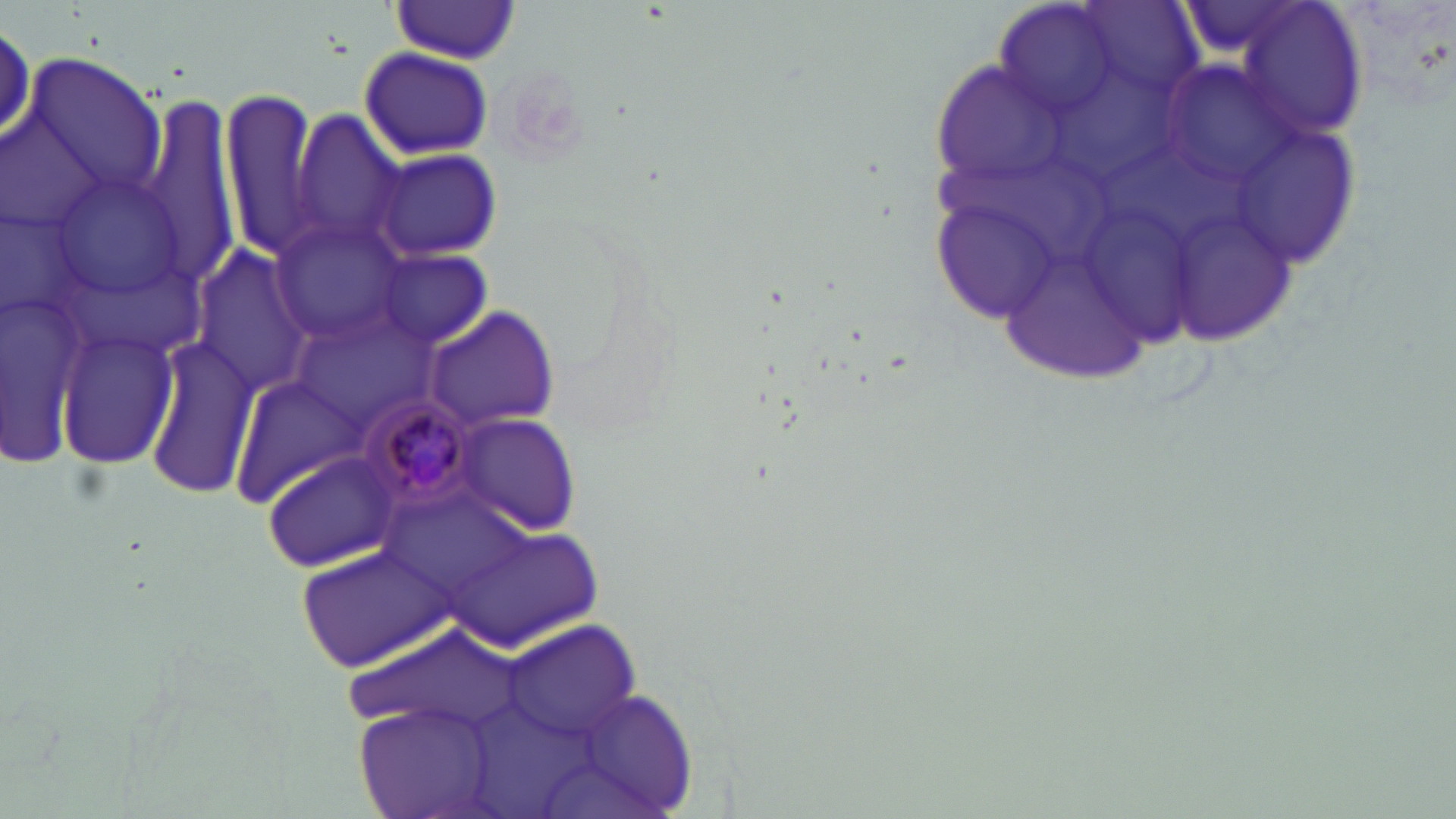 Approximate bounding boxes as (x1,y1)-(x2,y2) corner pairs in pixels. Plasmodium malariae-infected red blood cell locations: (357,390)-(484,510). Uninfected red blood cell locations: (1225,0)-(1367,142), (385,3)-(524,64), (359,47)-(493,160), (23,53)-(164,204), (141,90)-(241,274), (220,90)-(325,262), (290,110)-(410,257), (370,146)-(504,262), (933,197)-(1064,323), (270,217)-(411,340), (190,244)-(315,396), (374,250)-(495,348), (424,306)-(560,429), (56,327)-(180,467), (144,338)-(261,498), (231,372)-(365,506), (451,412)-(583,535), (262,448)-(406,571), (440,530)-(608,655), (298,541)-(452,674), (502,622)-(643,745), (557,685)-(699,819), (356,702)-(501,819). Slide-level diagnosis: Plasmodium malariae. May-Grünwald-Giemsa stain. Image is 1456×819 pixels. Single field of view. Thin blood film. 1000x magnification. Light microscopy.